Identify the parasite.
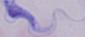
A trypanosome.

1000x magnification. Micrograph.